Outline each blood parasite and name the species.
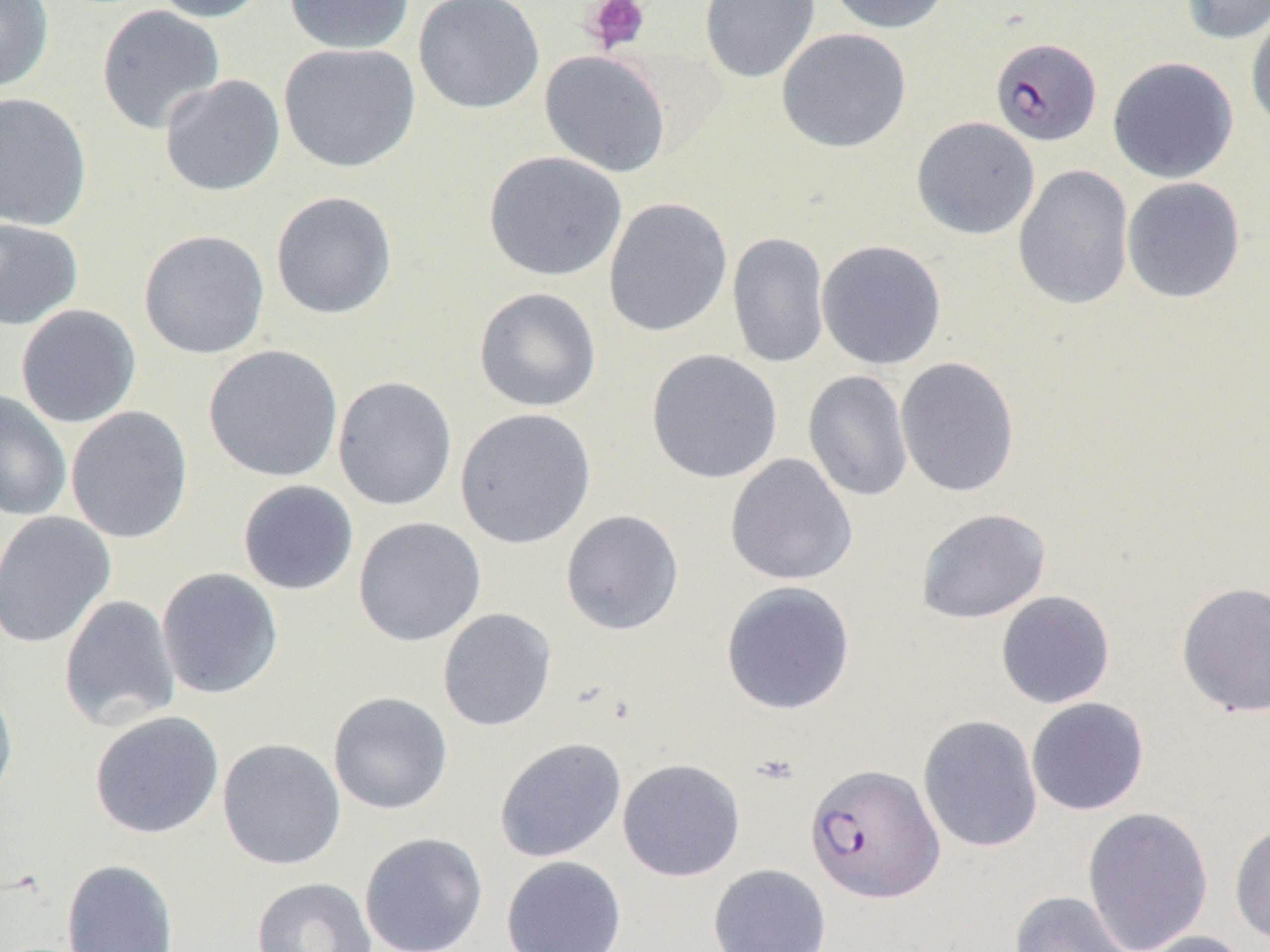

Approximate bounding boxes as (x1, y1, x2, y2) in pixels.
Plasmodium falciparum-infected red blood cells: (990, 37, 1102, 146), (805, 763, 943, 902).
No Plasmodium ovale, Plasmodium malariae, Plasmodium vivax, Babesia divergens, or Trypanosoma brucei observed.

Uninfected red blood cell locations: (0, 0, 54, 94), (151, 0, 271, 23), (283, 0, 415, 55), (413, 0, 546, 115), (699, 0, 820, 84), (825, 0, 953, 35), (1179, 0, 1269, 45), (95, 4, 226, 136), (1245, 7, 1270, 136), (776, 28, 912, 153), (278, 42, 421, 173), (539, 50, 672, 178), (1107, 56, 1238, 183), (159, 74, 286, 198), (0, 92, 93, 231), (910, 116, 1040, 240), (483, 151, 628, 282), (1013, 164, 1134, 310), (1122, 177, 1246, 303), (270, 191, 398, 320), (603, 197, 733, 338), (0, 217, 84, 330), (138, 229, 270, 360), (727, 231, 829, 370), (817, 239, 947, 370), (473, 287, 602, 412), (15, 304, 142, 428), (203, 344, 344, 483), (646, 350, 783, 484), (895, 356, 1020, 498), (803, 370, 913, 502), (332, 375, 458, 511), (0, 390, 72, 522), (66, 405, 194, 544), (455, 408, 596, 549), (725, 453, 857, 586), (237, 480, 359, 596), (915, 508, 1051, 624), (0, 510, 116, 650), (560, 510, 684, 636), (352, 517, 486, 647), (156, 567, 284, 700), (720, 581, 855, 715), (1176, 581, 1270, 717), (996, 591, 1115, 709), (58, 595, 181, 731), (437, 608, 557, 732), (0, 680, 18, 811), (327, 691, 453, 815), (1026, 697, 1149, 816), (88, 710, 224, 839), (918, 715, 1043, 852), (494, 737, 627, 863), (217, 738, 346, 871), (617, 758, 745, 881), (1082, 806, 1213, 952), (1230, 821, 1270, 946), (359, 831, 489, 952), (500, 856, 627, 951), (61, 859, 179, 952), (708, 864, 832, 952), (251, 877, 377, 952), (1009, 891, 1134, 952), (1132, 930, 1256, 952). Platelet locations: (582, 0, 651, 53). Slide-level diagnosis: Plasmodium falciparum. Captured at 1000x magnification. Light microscopy. Thin blood film. Single field of view. Image is 1270×952 pixels.